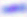

Summary:
  - Magnification: 400x
  - Identification: Toxoplasma gondii
  - Modality: micrograph